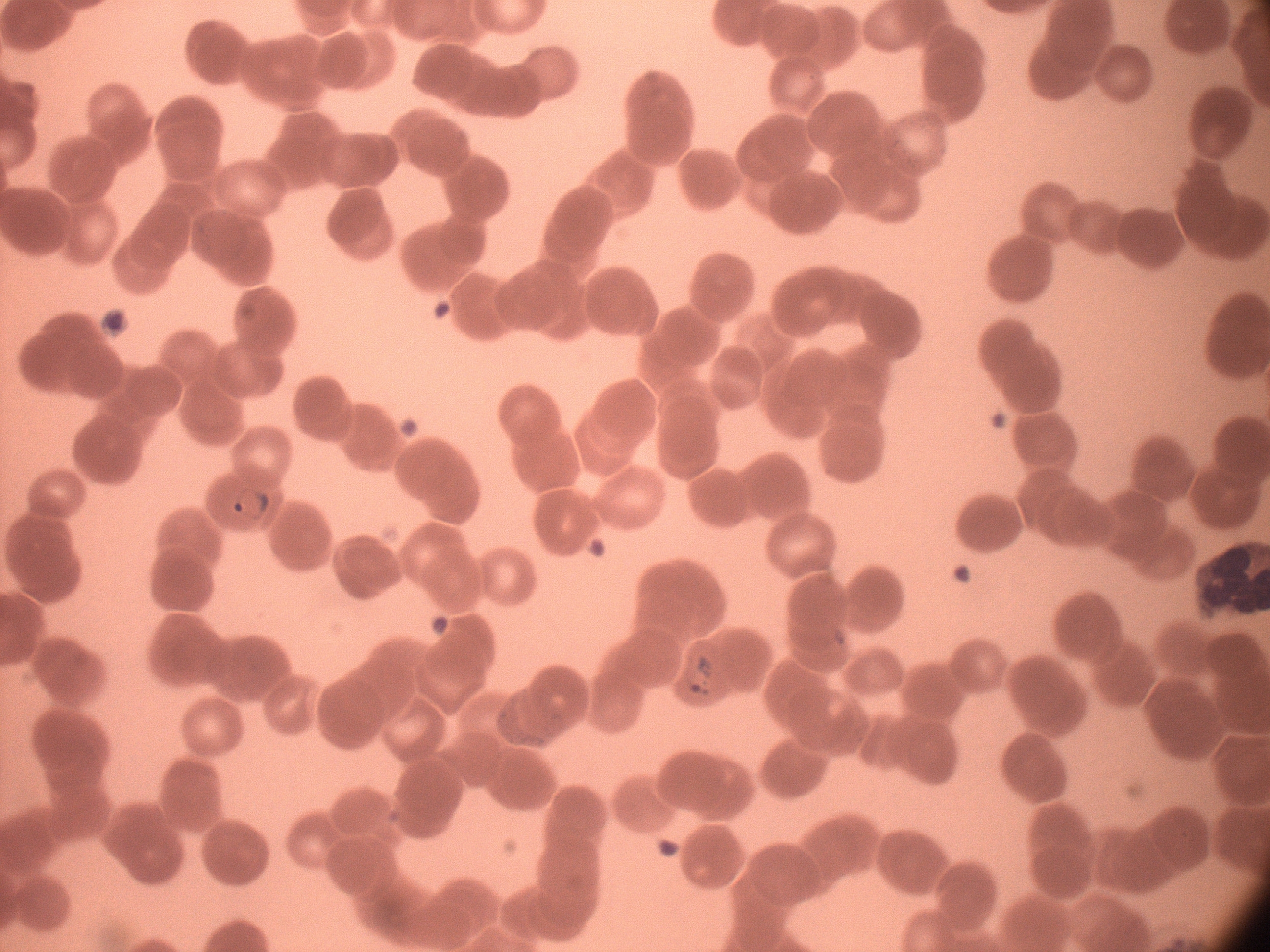

Approximate bounding boxes as (x1, y1, x2, y2) in pixels, from the source annotation, which is not necessarily exhaustive. Ring form locations: (227, 483, 276, 524), (681, 650, 719, 700). Image is 1270×952 pixels. Thin blood film. Giemsa stain. 100x magnification. One field from this slide. Acquired with a Leica DM2000 optical microscope and its built-in camera. Species: Plasmodium falciparum.